Report the malaria status of this cell.
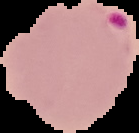
It is parasitized.

From a thin blood smear. Image is 139×133 pixels. The area outside the segmented cell region is set to black.